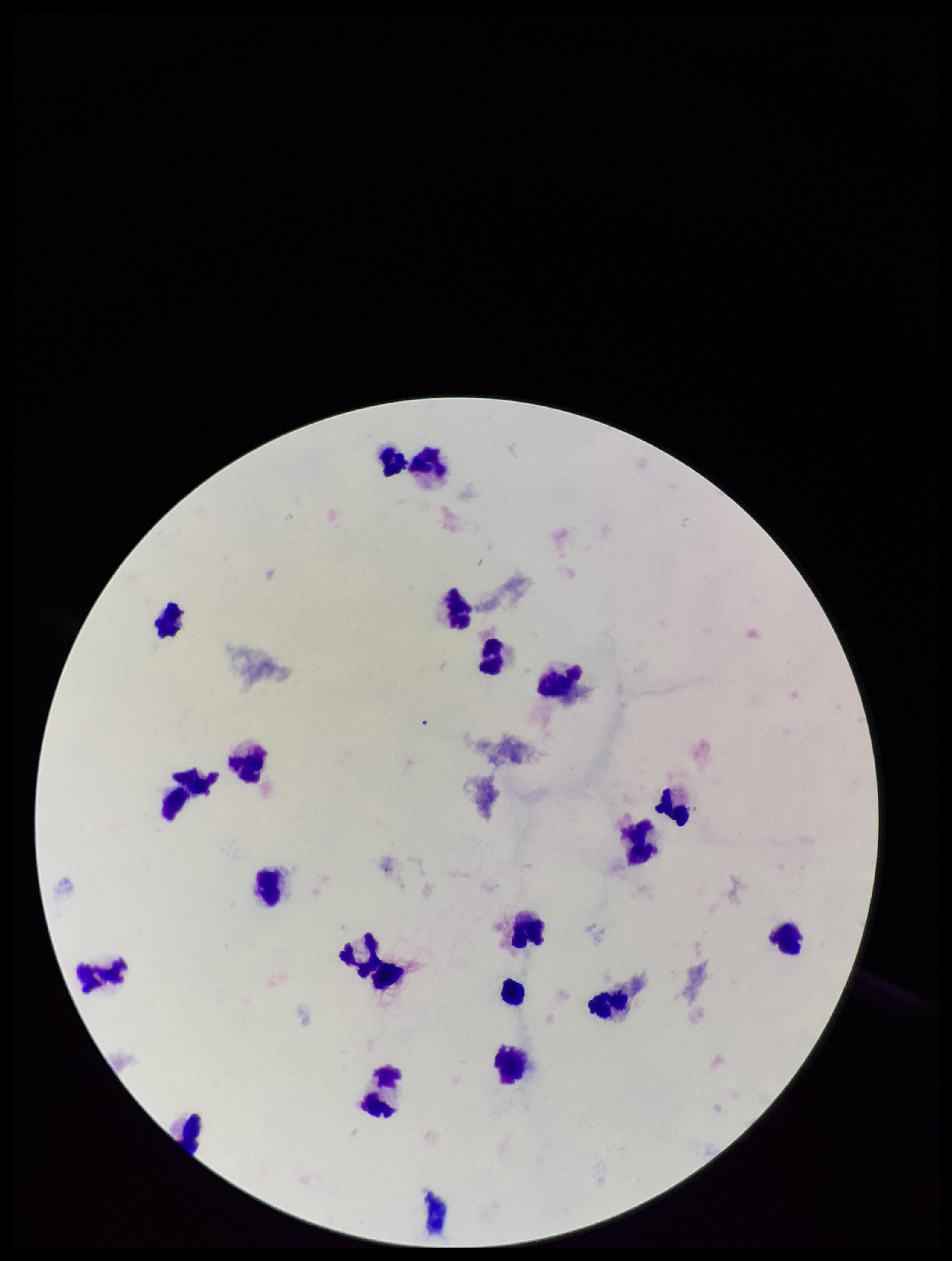

parasite count = 0
capture = smartphone photograph through the microscope eyepiece
field of view = single
image size = 952×1261 pixels
patient malaria status = negative
stain = Giemsa
preparation = thick smear
Plasmodium parasites = none identified
leukocyte count = 20